Describe the morphology of the erythrocytes.
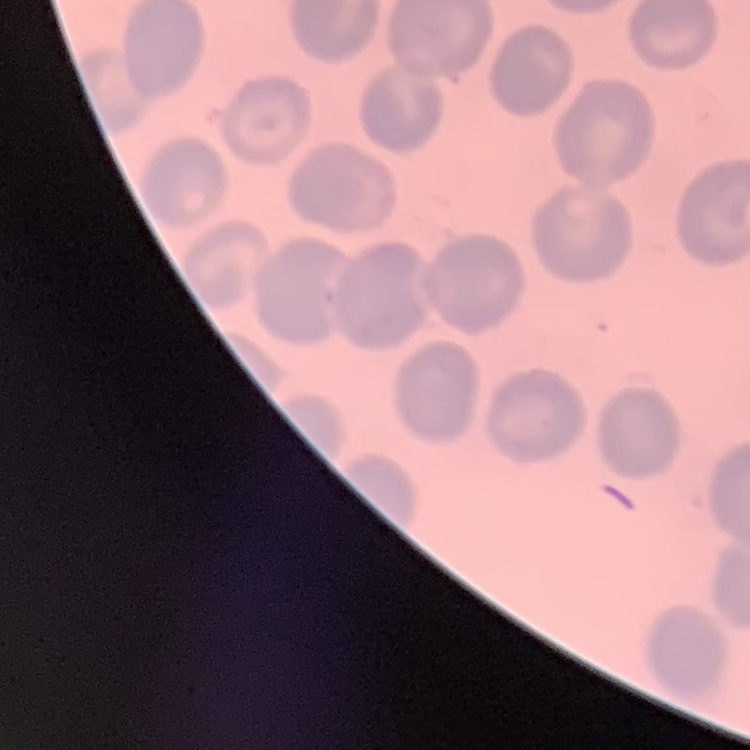
No rouleaux formation.

{
  "image_type": "square crop of a larger photomicrograph",
  "stain": "Field's or Giemsa",
  "preparation": "thin peripheral smear"
}